Classify this cell by malaria status.
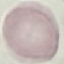

It is uninfected.

stain = Giemsa
preparation = thin blood film
image type = automatically extracted cell patch, resized to 64 × 64 pixels
capture = smartphone through the microscope eyepiece